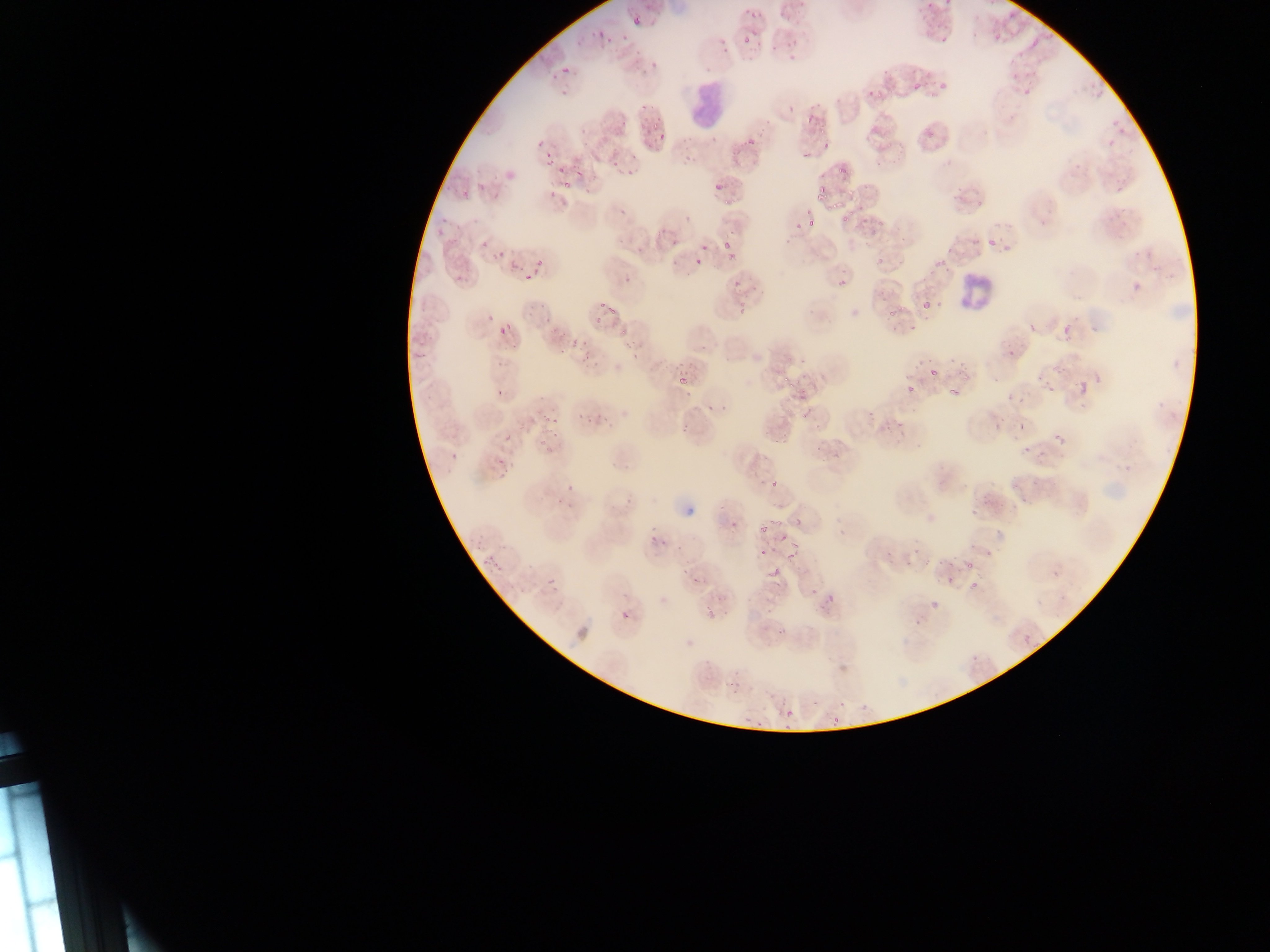

Approximate bounding boxes as (left, top, right, bottom) in pixels. Leukocyte locations: (691, 82, 734, 132), (959, 275, 995, 316). Plasmodium parasite locations (subset; some below the resolvable size): (633, 16, 642, 26), (597, 31, 605, 40), (574, 38, 585, 44), (1031, 39, 1039, 48), (633, 43, 642, 58), (650, 62, 658, 72), (562, 69, 570, 74), (913, 83, 920, 91), (878, 89, 886, 98), (820, 126, 828, 136), (538, 137, 547, 148), (647, 139, 654, 147), (748, 139, 756, 148), (542, 152, 555, 166), (802, 152, 809, 161), (571, 155, 584, 167), (613, 159, 621, 167), (837, 161, 852, 172), (575, 171, 583, 178), (714, 183, 721, 191), (815, 187, 826, 197), (829, 199, 840, 209), (618, 203, 631, 215), (807, 216, 818, 228), (721, 240, 732, 248), (481, 241, 489, 247), (985, 241, 993, 247), (700, 244, 708, 253), (500, 249, 504, 257), (877, 258, 885, 265), (537, 259, 545, 266), (508, 262, 517, 273), (934, 262, 944, 270), (523, 274, 531, 282), (623, 275, 633, 282), (923, 300, 930, 309), (598, 301, 605, 309), (735, 302, 746, 317), (607, 306, 615, 318), (885, 309, 896, 324), (527, 311, 535, 319), (594, 314, 605, 324), (543, 317, 551, 327), (1029, 324, 1036, 333), (621, 327, 627, 335), (498, 328, 508, 334), (549, 328, 557, 336), (560, 329, 568, 340), (571, 338, 576, 349), (581, 338, 587, 347), (620, 339, 635, 347), (558, 346, 564, 354), (631, 349, 639, 358), (578, 356, 586, 365), (931, 367, 939, 378), (676, 370, 692, 386), (781, 375, 789, 383), (1076, 380, 1088, 395), (906, 383, 915, 394), (1047, 385, 1056, 394), (946, 388, 957, 395), (684, 393, 692, 398), (707, 403, 713, 411), (719, 403, 726, 412), (575, 413, 582, 421), (587, 413, 593, 424), (544, 414, 550, 424), (551, 417, 559, 424), (813, 417, 823, 432), (551, 426, 562, 439), (505, 430, 513, 443), (450, 449, 461, 458), (502, 468, 509, 478), (770, 479, 778, 488), (566, 480, 577, 491), (624, 497, 636, 506), (556, 498, 561, 506), (567, 498, 574, 506), (717, 505, 726, 514), (773, 519, 783, 527), (730, 523, 735, 531), (759, 523, 767, 533), (777, 531, 789, 543), (650, 533, 657, 543), (661, 537, 668, 547), (675, 542, 683, 550), (759, 545, 772, 557), (786, 550, 796, 562), (486, 556, 498, 568), (489, 558, 502, 569), (968, 560, 976, 569), (768, 564, 782, 579), (682, 566, 689, 575), (1051, 569, 1060, 578), (690, 573, 700, 589), (547, 577, 557, 588), (970, 580, 977, 588), (619, 610, 630, 620), (1024, 636, 1032, 644), (785, 709, 793, 718) | approximate (x, y) pixel centers of objects too small to bound: (592, 34), (624, 37), (608, 41), (642, 106), (647, 120), (663, 138), (586, 191), (726, 201), (687, 219), (844, 220), (673, 244), (639, 250), (494, 257), (698, 262), (543, 304), (490, 319), (793, 385), (500, 392), (803, 414), (685, 426), (502, 461), (709, 606). Collected in Ghana. Thin blood smear. Photographed through a microscope with a mobile-phone camera. Image is 1270×952 pixels. Single field of view.